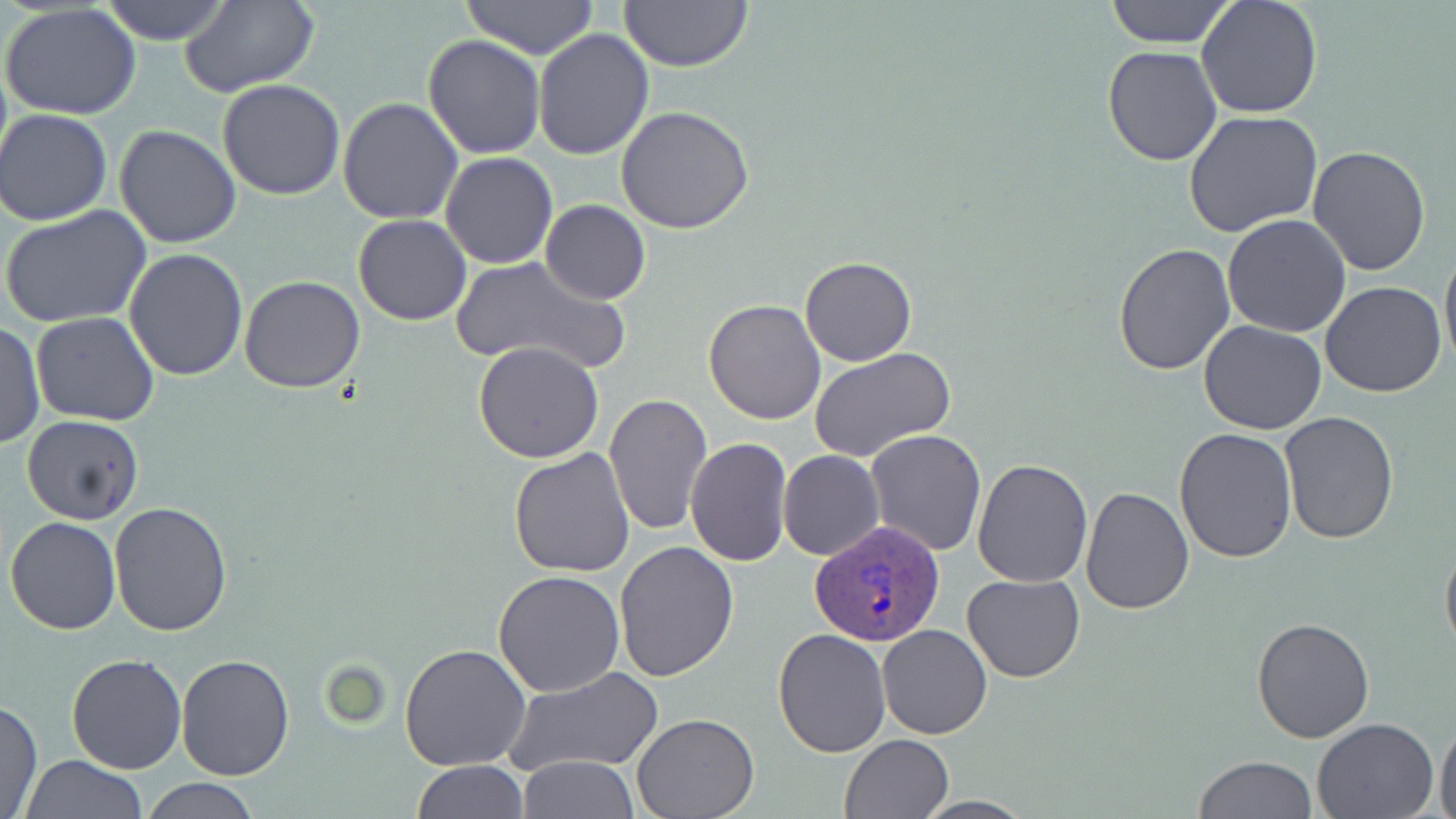

Approximate bounding boxes as named x1/y1/x2/y2 corners in pixels. Uninfected red blood cell locations: (x1=99, y1=0, x2=232, y2=45), (x1=459, y1=0, x2=600, y2=56), (x1=616, y1=0, x2=753, y2=72), (x1=1102, y1=0, x2=1237, y2=48), (x1=1197, y1=0, x2=1324, y2=121), (x1=178, y1=2, x2=318, y2=95), (x1=1, y1=4, x2=141, y2=120), (x1=1102, y1=23, x2=1306, y2=148), (x1=532, y1=28, x2=655, y2=159), (x1=423, y1=33, x2=544, y2=158), (x1=1101, y1=45, x2=1223, y2=166), (x1=218, y1=80, x2=346, y2=201), (x1=337, y1=96, x2=464, y2=225), (x1=615, y1=104, x2=755, y2=232), (x1=1, y1=108, x2=116, y2=225), (x1=1183, y1=110, x2=1323, y2=237), (x1=113, y1=124, x2=240, y2=249), (x1=1308, y1=145, x2=1432, y2=278), (x1=441, y1=152, x2=559, y2=269), (x1=540, y1=200, x2=650, y2=304), (x1=1, y1=204, x2=152, y2=329), (x1=352, y1=213, x2=471, y2=325), (x1=1222, y1=213, x2=1351, y2=338), (x1=1440, y1=237, x2=1456, y2=372), (x1=1113, y1=243, x2=1234, y2=375), (x1=125, y1=247, x2=248, y2=382), (x1=449, y1=255, x2=631, y2=377), (x1=800, y1=257, x2=918, y2=367), (x1=238, y1=274, x2=364, y2=392), (x1=1319, y1=281, x2=1449, y2=398), (x1=704, y1=298, x2=827, y2=424), (x1=30, y1=312, x2=159, y2=426), (x1=1, y1=319, x2=44, y2=451), (x1=1199, y1=321, x2=1327, y2=436), (x1=472, y1=341, x2=605, y2=464), (x1=810, y1=345, x2=959, y2=463), (x1=604, y1=391, x2=713, y2=536), (x1=1280, y1=411, x2=1399, y2=544), (x1=22, y1=416, x2=144, y2=525), (x1=1173, y1=426, x2=1297, y2=563), (x1=864, y1=428, x2=986, y2=557), (x1=685, y1=438, x2=792, y2=568), (x1=509, y1=448, x2=636, y2=578), (x1=779, y1=451, x2=885, y2=561), (x1=972, y1=459, x2=1093, y2=587), (x1=1079, y1=485, x2=1194, y2=614), (x1=109, y1=501, x2=233, y2=636), (x1=5, y1=517, x2=122, y2=635), (x1=1440, y1=533, x2=1456, y2=663), (x1=613, y1=541, x2=739, y2=682), (x1=494, y1=571, x2=625, y2=697), (x1=961, y1=573, x2=1085, y2=683), (x1=1251, y1=615, x2=1377, y2=742), (x1=877, y1=623, x2=992, y2=740), (x1=772, y1=628, x2=890, y2=759), (x1=400, y1=644, x2=531, y2=771), (x1=65, y1=653, x2=188, y2=774), (x1=175, y1=654, x2=295, y2=781), (x1=502, y1=665, x2=665, y2=777), (x1=1, y1=700, x2=42, y2=819), (x1=631, y1=713, x2=760, y2=819), (x1=1313, y1=717, x2=1440, y2=818), (x1=1435, y1=719, x2=1456, y2=819), (x1=840, y1=734, x2=952, y2=819), (x1=20, y1=755, x2=148, y2=818), (x1=1194, y1=755, x2=1316, y2=819), (x1=518, y1=756, x2=640, y2=817), (x1=412, y1=760, x2=529, y2=818), (x1=138, y1=777, x2=262, y2=817), (x1=910, y1=797, x2=1038, y2=818). Plasmodium ovale-infected red blood cell locations: (x1=811, y1=519, x2=942, y2=647). Slide-level diagnosis: Plasmodium ovale. One field of a larger specimen. May-Grünwald-Giemsa-stained preparation. Thin blood film. 1000x magnification. Optical microscopy. Image is 1456×819 pixels.